Point out each Plasmodium parasite and each leukocyte.
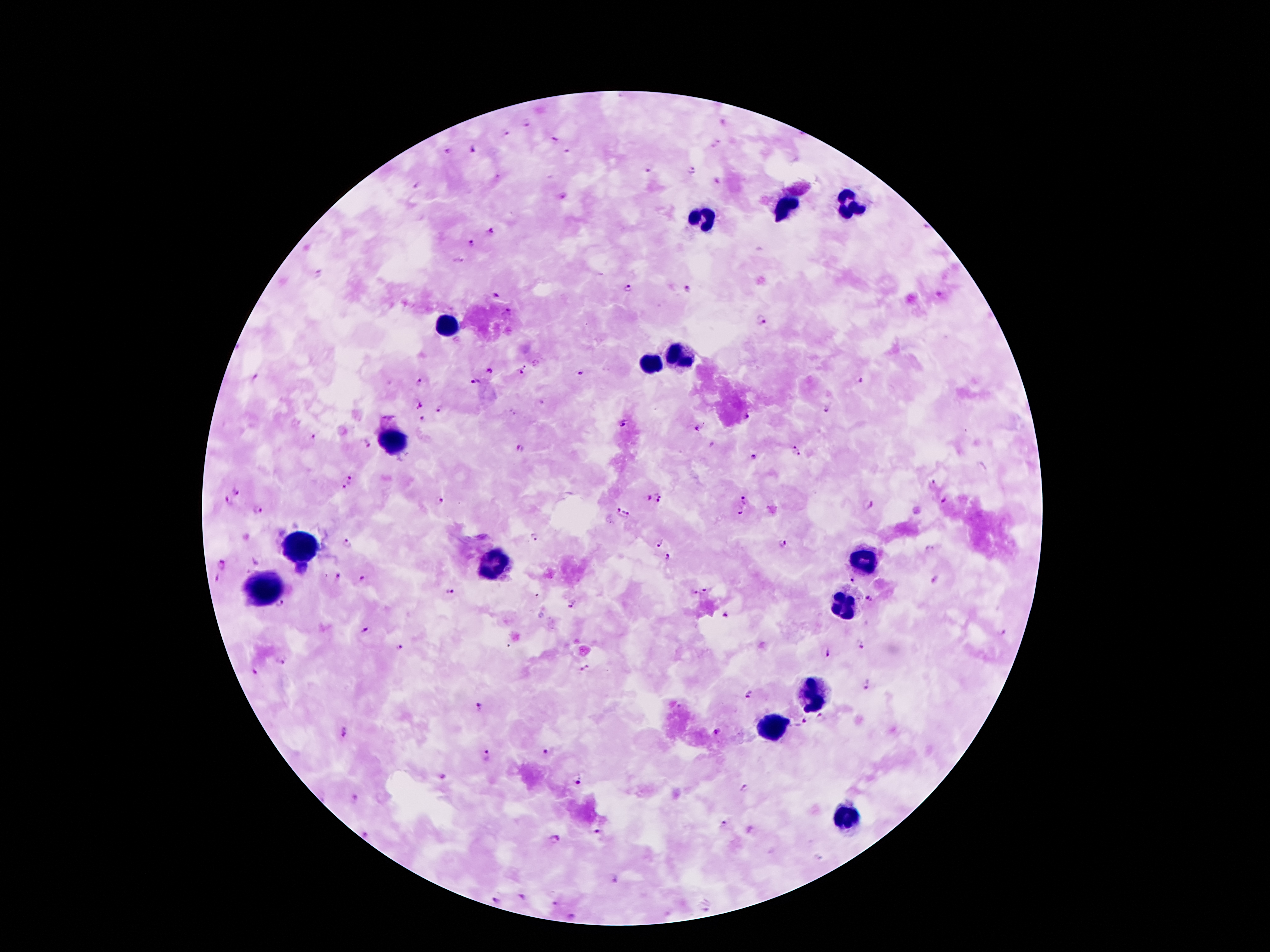
Approximate centers as [x, y] in pixels.
Plasmodium parasites: [525, 123], [505, 134], [553, 138], [473, 150], [565, 150], [446, 151], [648, 170], [690, 170], [414, 185], [561, 194], [927, 228], [491, 231], [471, 243], [459, 261], [629, 289], [687, 289], [497, 294], [762, 321], [526, 370], [490, 371], [579, 371], [257, 379], [861, 379], [419, 381], [475, 381], [420, 405], [440, 408], [827, 410], [749, 418], [422, 420], [623, 422], [697, 428], [313, 437], [365, 443], [712, 444], [794, 446], [520, 449], [799, 454], [754, 457], [351, 479], [934, 482], [343, 487], [236, 492], [660, 494], [647, 497], [439, 500], [656, 500], [745, 500], [229, 501], [946, 501], [867, 505], [258, 510], [617, 510], [626, 511], [738, 511], [532, 538], [347, 544], [658, 544], [782, 544], [931, 550], [668, 557], [222, 566], [337, 576], [216, 579], [363, 579], [935, 580], [852, 581], [704, 589], [450, 591], [692, 591], [869, 599], [573, 603], [281, 605], [725, 616], [365, 630], [1004, 632], [861, 643], [398, 647], [825, 653], [282, 658], [586, 669], [254, 671], [865, 686], [748, 693], [480, 707], [821, 719], [800, 723], [716, 731], [345, 733], [550, 751], [486, 754], [441, 778], [579, 779], [744, 789], [354, 798], [725, 825], [600, 834], [367, 836], [552, 838], [612, 879], [522, 897], [496, 899], [554, 903], [704, 907], [575, 916].
Leukocytes: [850, 204], [788, 205], [705, 217], [446, 324], [677, 357], [652, 366], [398, 435], [301, 544], [863, 558], [493, 566], [267, 586], [845, 606], [813, 694], [773, 729], [845, 821].

{
  "capture": "smartphone camera through the microscope eyepiece",
  "preparation": "thick blood smear",
  "stain": "Giemsa",
  "patient_malaria_status": "infected with Plasmodium falciparum",
  "image_size": "1270×952 pixels",
  "field_of_view": "single",
  "magnification": "100x"
}